Identify the blood parasite species.
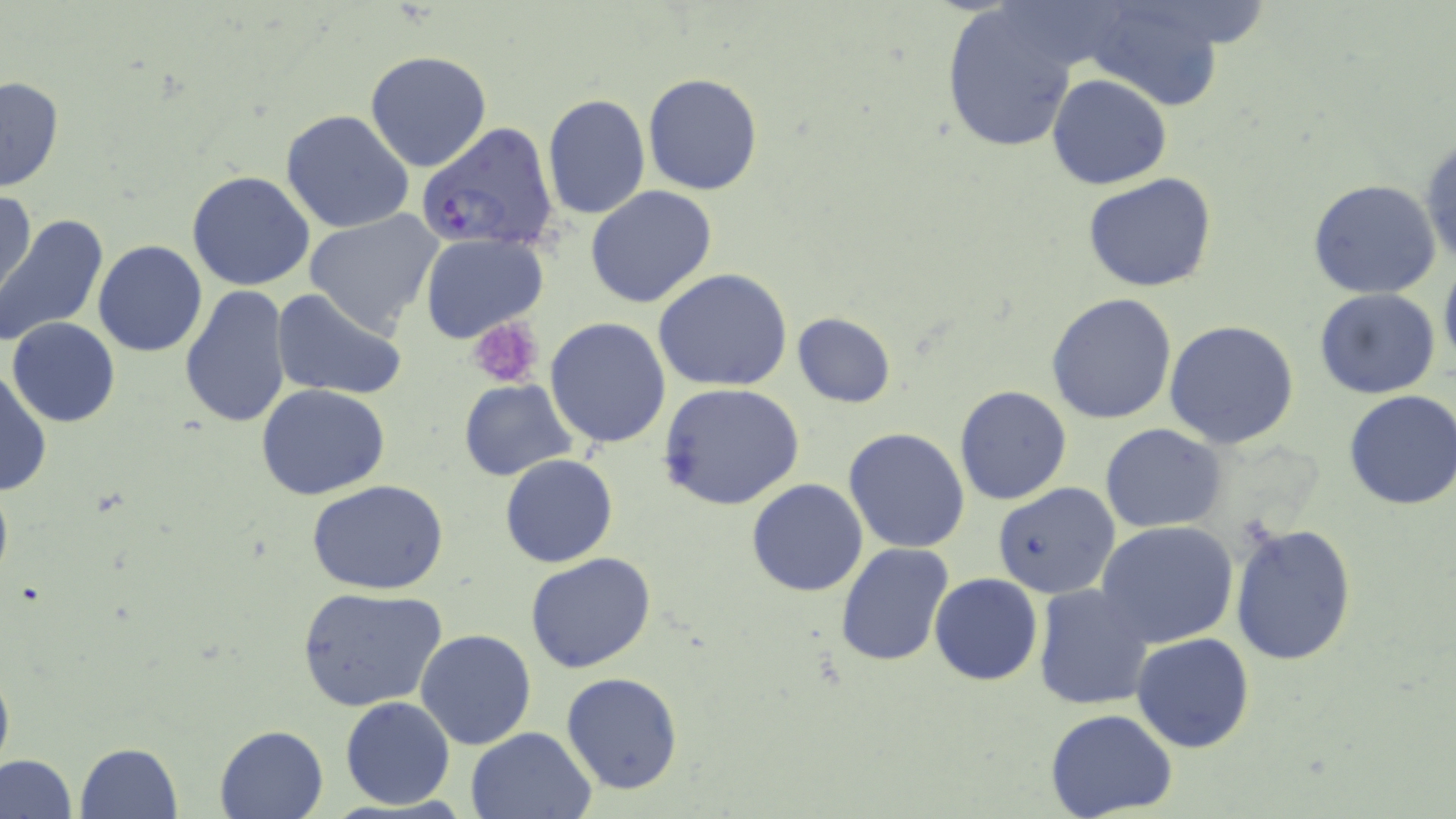
Plasmodium falciparum.

Approximate bounding boxes as [x1, y1, x2, y2] in pixels. Platelet locations: [468, 318, 545, 388]. Uninfected red blood cell locations: [1079, 0, 1231, 111], [942, 6, 1078, 153], [365, 50, 493, 173], [642, 73, 763, 194], [1047, 74, 1173, 190], [0, 75, 65, 194], [541, 94, 651, 219], [281, 109, 416, 235], [1419, 135, 1455, 273], [187, 171, 316, 292], [1083, 172, 1219, 293], [1308, 179, 1442, 299], [585, 186, 718, 310], [1, 187, 36, 309], [303, 209, 444, 335], [0, 213, 108, 349], [420, 232, 547, 343], [92, 239, 208, 359], [1438, 254, 1456, 380], [653, 270, 794, 392], [179, 285, 292, 429], [1314, 288, 1442, 399], [272, 290, 406, 401], [1047, 292, 1179, 426], [792, 312, 896, 408], [8, 318, 120, 428], [545, 318, 671, 450], [1164, 320, 1299, 449], [0, 367, 52, 497], [459, 380, 578, 481], [658, 382, 805, 509], [257, 383, 389, 500], [953, 384, 1072, 506], [1343, 389, 1456, 512], [1100, 423, 1224, 533], [842, 428, 970, 553], [500, 454, 618, 568], [747, 479, 868, 597], [308, 480, 449, 595], [992, 481, 1120, 599], [1096, 520, 1240, 648], [1229, 522, 1358, 666], [835, 543, 955, 668], [526, 553, 657, 675], [930, 573, 1043, 687], [1032, 584, 1154, 710], [298, 587, 448, 715], [415, 629, 538, 750], [1132, 631, 1255, 753], [0, 652, 14, 785], [561, 671, 684, 795], [339, 696, 456, 810], [1046, 709, 1178, 819], [214, 725, 329, 818], [465, 727, 595, 818], [74, 742, 183, 819], [0, 754, 77, 819]. Plasmodium falciparum-infected red blood cell locations: [417, 122, 560, 254]. Captured at 1000x magnification. May-Grünwald-Giemsa-stained preparation. Image is 1456×819 pixels. Light microscopy. One field of a larger specimen. Thin blood smear.